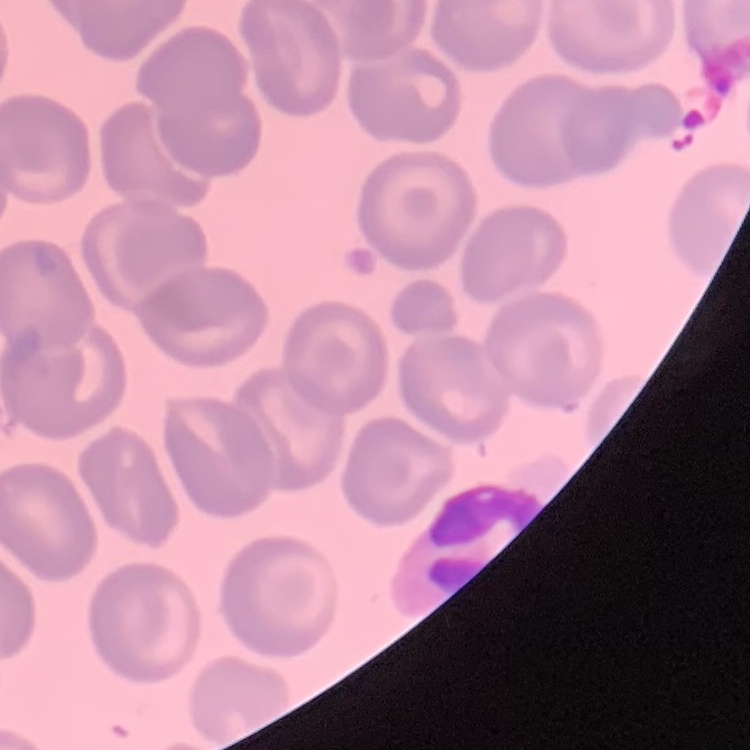

Summary:
  - Red blood cell morphology: no rouleaux formation
  - Image type: square crop of a larger photomicrograph
  - Preparation: thin blood smear
  - Stain: Field's or Giemsa